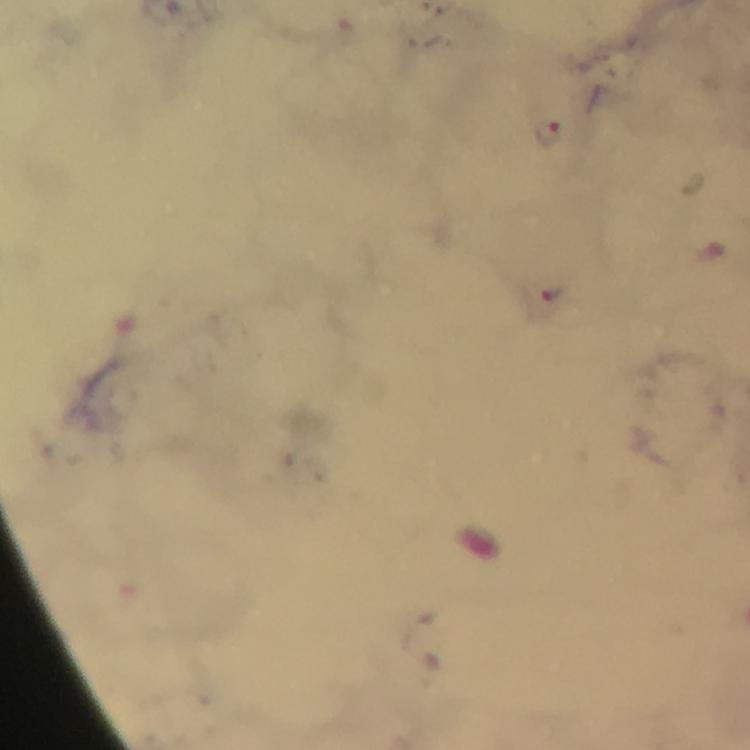
Approximate centers as [x, y] in pixels.
Summary:
  - Malaria parasite locations: [547, 132]
  - Cropped from: a single field of view
  - Stain: Giemsa
  - Preparation: thick smear
  - Capture: smartphone photograph through a microscope
  - Context: from a diagnostic examination for malaria
  - Magnification: 100x
  - Image size: 750×750 pixels
  - Immersion oil: applied